Report the malaria status of this cell.
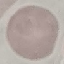
Uninfected.

Summary:
  - Stain: Giemsa
  - Capture: smartphone through the microscope eyepiece
  - Preparation: thin smear
  - Image type: automatically extracted cell patch, resized to 64 × 64 pixels